Report the malaria status of this cell.
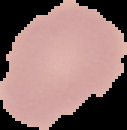

Uninfected.

{
  "image_size": "127×130 pixels",
  "preparation": "thin blood film",
  "image_type": "segmented cell region with the area outside set to black"
}